Point out each Plasmodium parasite and classify it by life-cycle stage.
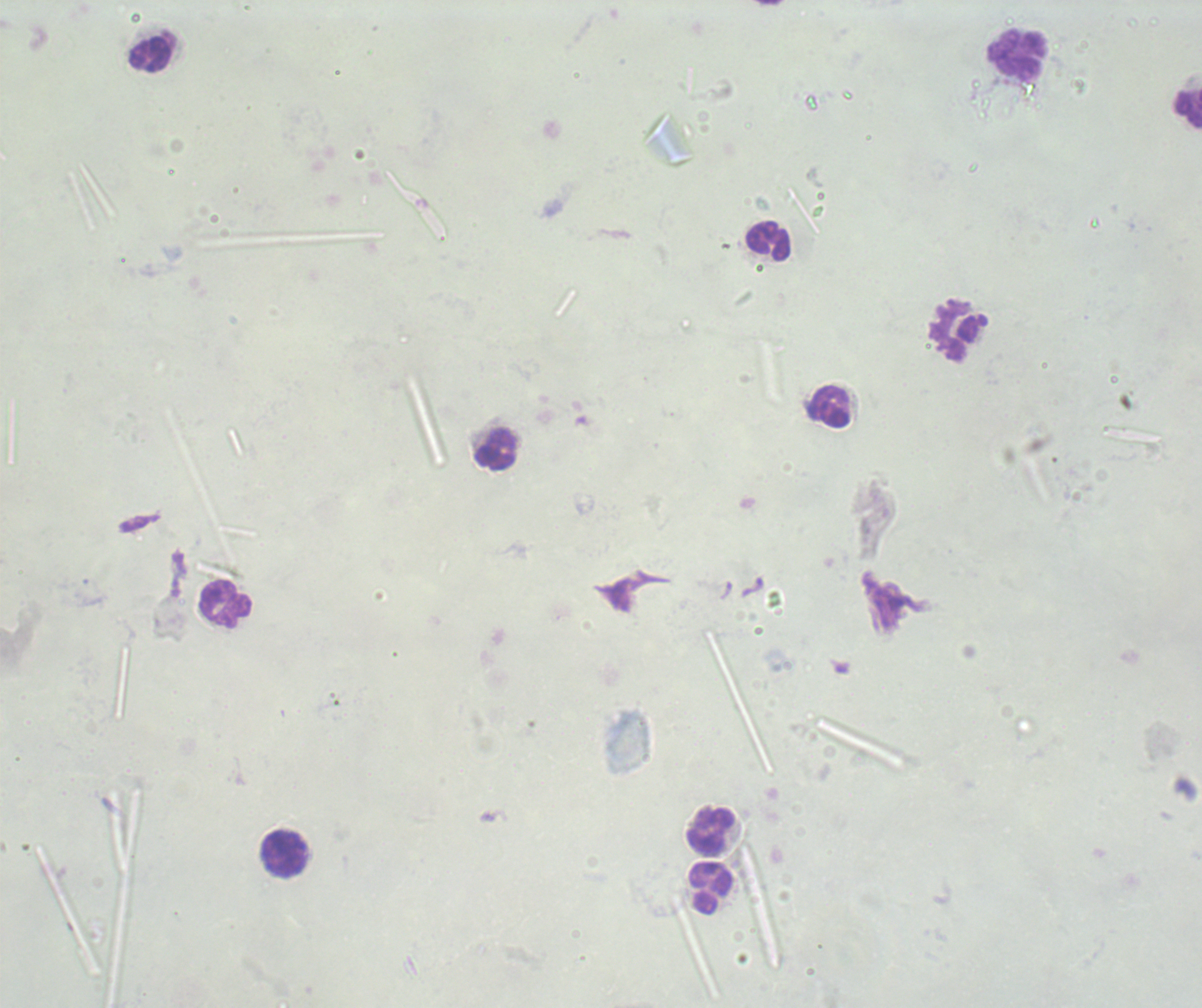

No Plasmodium parasites detected.

Approximate object centers, in pixels from the top-left corner.
Summary:
  - Leukocyte locations: (x=149, y=53), (x=1017, y=53), (x=1188, y=110), (x=768, y=243), (x=955, y=332), (x=829, y=406), (x=495, y=449), (x=225, y=604), (x=711, y=831), (x=284, y=855), (x=711, y=890)
  - Magnification: 100x
  - Image size: 1202×1008 pixels
  - Context: previously used in a real diagnosis
  - Preparation: thick blood smear
  - Stain: Romanowsky
  - Background quality: unsatisfactory
  - Field of view: one from this slide